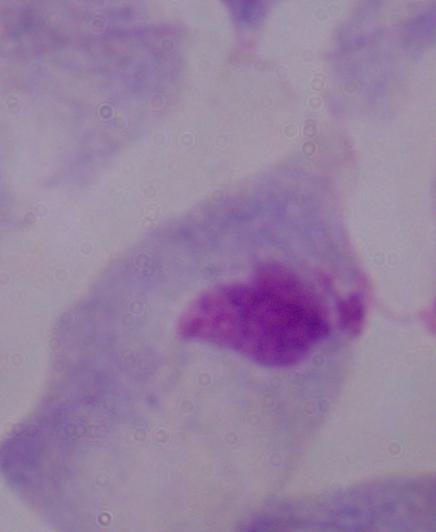
magnification = 1000x
modality = micrograph
identification = trichomonad